Comment on the morphology of the erythrocytes.
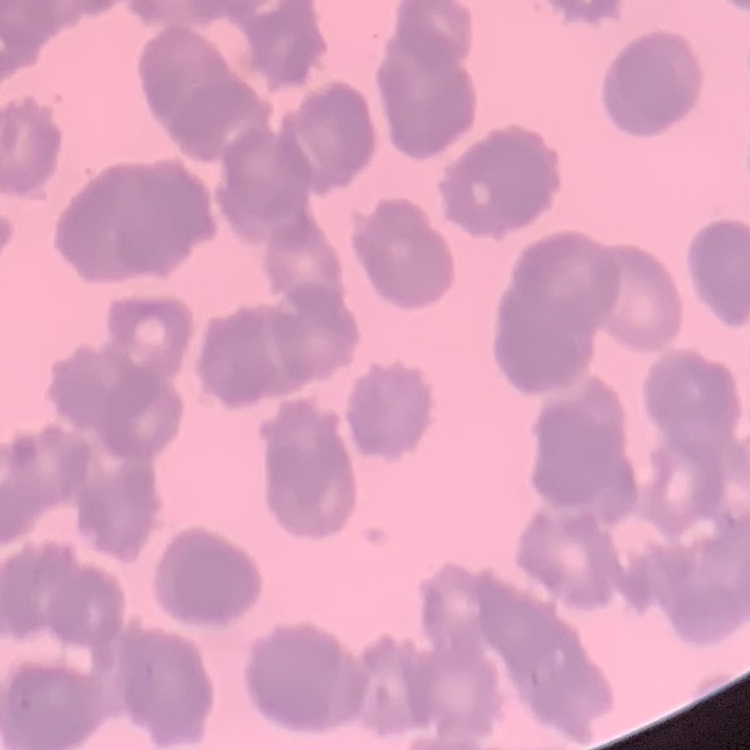
They show rouleaux formation.

image type = one tile cut from a larger photomicrograph
stain = Field's or Giemsa
preparation = thin peripheral smear